Describe the morphology of the red blood cells.
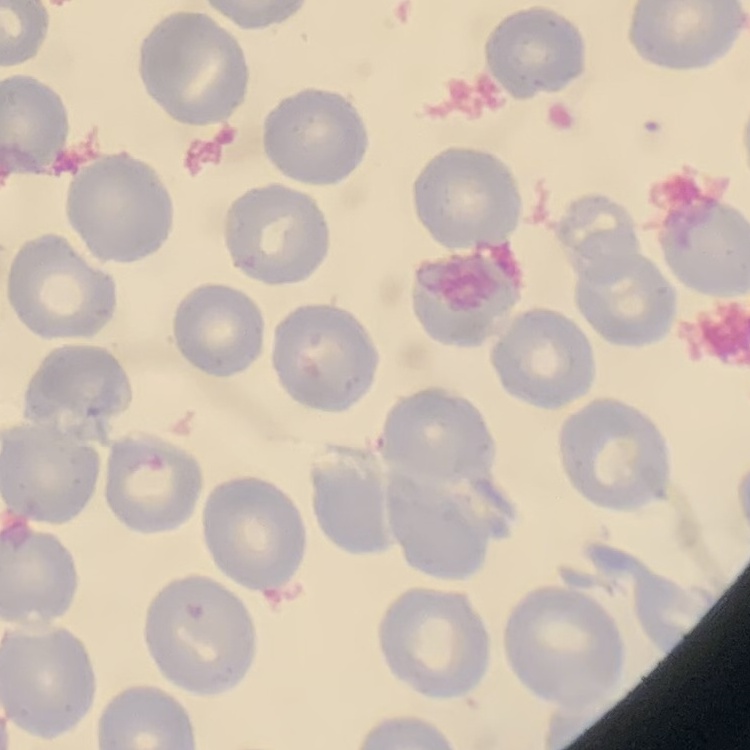
No rouleaux formation.

{
  "preparation": "thin peripheral smear",
  "image_type": "one tile cut from a larger photomicrograph",
  "stain": "Field's or Giemsa"
}